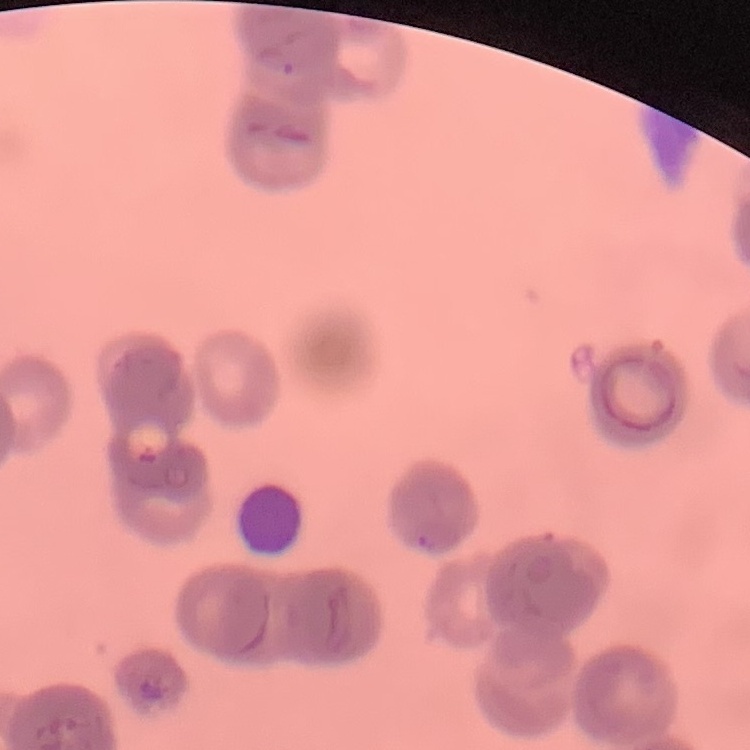

The red blood cells show rouleaux formation. Thin peripheral smear. Square crop of a larger photomicrograph. Stained with either Field's or Giemsa.